Locate every Plasmodium falciparum-infected red blood cell.
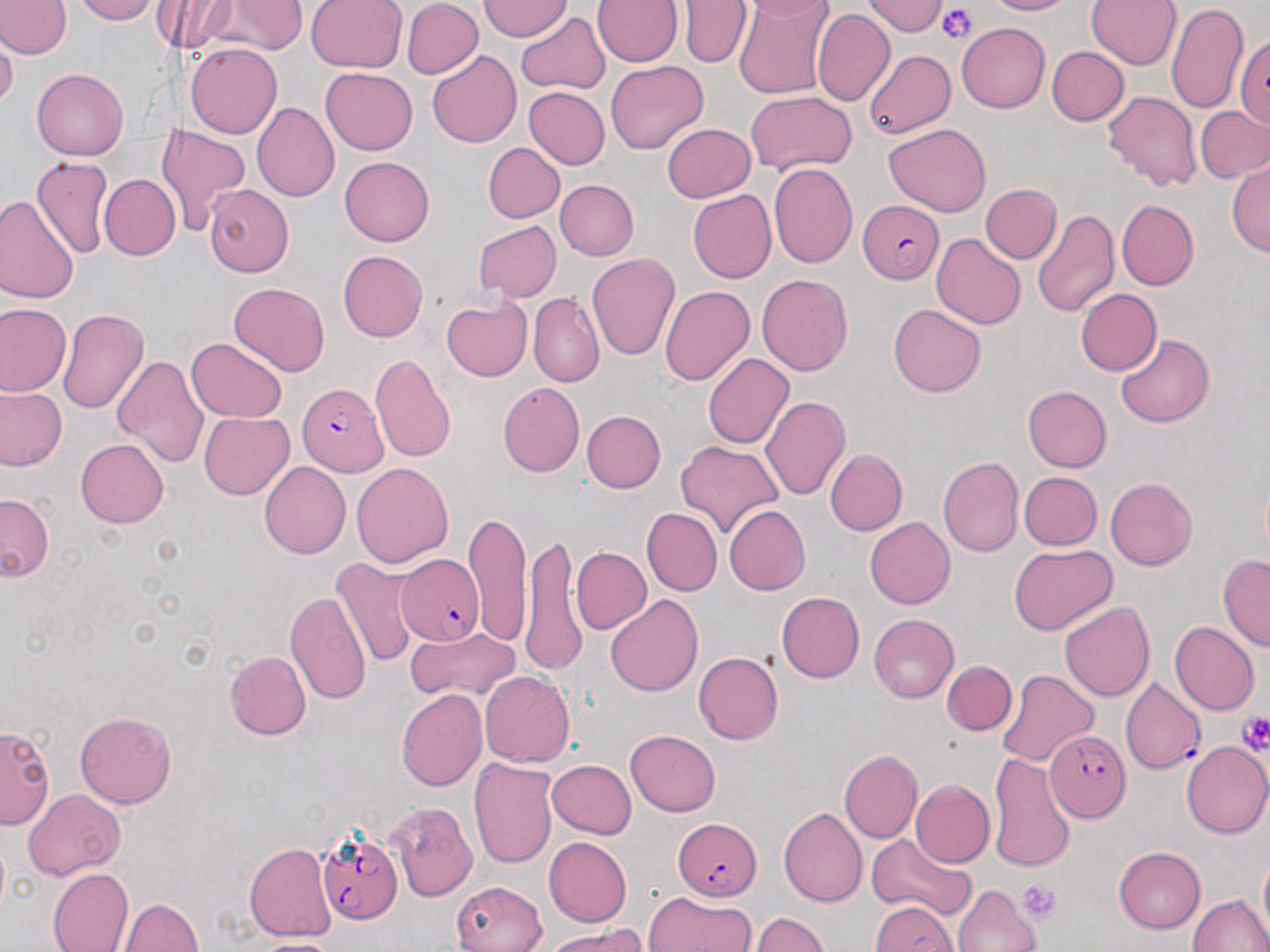
Approximate bounding boxes as named x1/y1/x2/y2 corners in pixels.
Plasmodium falciparum-infected red blood cells: (x1=855, y1=198, x2=942, y2=282), (x1=295, y1=382, x2=388, y2=473), (x1=394, y1=555, x2=484, y2=648), (x1=1122, y1=679, x2=1205, y2=776), (x1=1044, y1=731, x2=1130, y2=820), (x1=675, y1=817, x2=762, y2=900), (x1=314, y1=828, x2=401, y2=924).

Summary:
  - Platelet locations: (x1=936, y1=7, x2=979, y2=44), (x1=1236, y1=707, x2=1270, y2=760), (x1=1021, y1=880, x2=1060, y2=924)
  - Uninfected red blood cell locations: (x1=72, y1=0, x2=162, y2=24), (x1=154, y1=0, x2=250, y2=52), (x1=221, y1=0, x2=304, y2=53), (x1=306, y1=0, x2=406, y2=74), (x1=480, y1=0, x2=572, y2=41), (x1=593, y1=0, x2=683, y2=67), (x1=731, y1=0, x2=834, y2=100), (x1=868, y1=0, x2=945, y2=36), (x1=983, y1=0, x2=1075, y2=17), (x1=1087, y1=0, x2=1179, y2=71), (x1=401, y1=1, x2=481, y2=78), (x1=681, y1=1, x2=750, y2=67), (x1=0, y1=2, x2=68, y2=59), (x1=1167, y1=5, x2=1250, y2=116), (x1=517, y1=10, x2=610, y2=93), (x1=812, y1=10, x2=893, y2=108), (x1=957, y1=23, x2=1051, y2=112), (x1=1235, y1=31, x2=1270, y2=132), (x1=0, y1=41, x2=16, y2=110), (x1=185, y1=44, x2=280, y2=139), (x1=1046, y1=45, x2=1128, y2=125), (x1=864, y1=49, x2=955, y2=140), (x1=427, y1=50, x2=523, y2=145), (x1=605, y1=61, x2=708, y2=153), (x1=32, y1=68, x2=129, y2=160), (x1=321, y1=69, x2=417, y2=154), (x1=522, y1=86, x2=607, y2=171), (x1=1100, y1=88, x2=1202, y2=192), (x1=743, y1=93, x2=856, y2=176), (x1=251, y1=103, x2=337, y2=203), (x1=1195, y1=104, x2=1270, y2=184), (x1=154, y1=122, x2=250, y2=238), (x1=661, y1=123, x2=756, y2=203), (x1=883, y1=123, x2=992, y2=216), (x1=482, y1=142, x2=563, y2=223), (x1=339, y1=156, x2=435, y2=247), (x1=31, y1=157, x2=114, y2=258), (x1=1227, y1=157, x2=1269, y2=258), (x1=770, y1=162, x2=858, y2=271), (x1=97, y1=174, x2=179, y2=261), (x1=554, y1=177, x2=637, y2=259), (x1=980, y1=183, x2=1061, y2=264), (x1=202, y1=185, x2=295, y2=276), (x1=689, y1=189, x2=776, y2=282), (x1=0, y1=195, x2=80, y2=306), (x1=1115, y1=200, x2=1197, y2=292), (x1=1032, y1=207, x2=1120, y2=320), (x1=472, y1=220, x2=560, y2=300), (x1=932, y1=232, x2=1026, y2=330), (x1=340, y1=249, x2=430, y2=342), (x1=586, y1=253, x2=681, y2=360), (x1=755, y1=271, x2=853, y2=378), (x1=229, y1=284, x2=330, y2=377), (x1=659, y1=284, x2=753, y2=385), (x1=1074, y1=288, x2=1160, y2=374), (x1=527, y1=292, x2=604, y2=388), (x1=442, y1=296, x2=531, y2=381), (x1=1, y1=302, x2=71, y2=397), (x1=888, y1=304, x2=988, y2=398), (x1=58, y1=306, x2=149, y2=418), (x1=1116, y1=333, x2=1216, y2=428), (x1=186, y1=338, x2=289, y2=423), (x1=702, y1=352, x2=794, y2=450), (x1=111, y1=353, x2=209, y2=469), (x1=370, y1=354, x2=456, y2=462), (x1=499, y1=382, x2=584, y2=476), (x1=1023, y1=386, x2=1113, y2=472), (x1=0, y1=387, x2=67, y2=473), (x1=762, y1=395, x2=851, y2=501), (x1=582, y1=410, x2=666, y2=492), (x1=197, y1=411, x2=294, y2=499), (x1=76, y1=439, x2=168, y2=527), (x1=675, y1=439, x2=784, y2=538), (x1=825, y1=448, x2=906, y2=535), (x1=936, y1=457, x2=1022, y2=558), (x1=352, y1=461, x2=453, y2=568), (x1=260, y1=462, x2=351, y2=558), (x1=1020, y1=472, x2=1101, y2=550), (x1=1104, y1=477, x2=1197, y2=570), (x1=0, y1=494, x2=54, y2=585), (x1=723, y1=504, x2=812, y2=595), (x1=642, y1=508, x2=722, y2=595), (x1=466, y1=513, x2=533, y2=643), (x1=866, y1=516, x2=955, y2=609), (x1=524, y1=535, x2=587, y2=677), (x1=1008, y1=543, x2=1117, y2=635), (x1=570, y1=545, x2=651, y2=635), (x1=1218, y1=554, x2=1269, y2=650), (x1=332, y1=556, x2=419, y2=673), (x1=284, y1=588, x2=373, y2=708), (x1=777, y1=591, x2=865, y2=682), (x1=606, y1=593, x2=702, y2=696), (x1=1058, y1=600, x2=1156, y2=703), (x1=866, y1=614, x2=958, y2=703), (x1=1170, y1=621, x2=1259, y2=713), (x1=403, y1=623, x2=523, y2=705), (x1=224, y1=651, x2=311, y2=740), (x1=694, y1=651, x2=784, y2=745), (x1=942, y1=661, x2=1016, y2=736), (x1=995, y1=669, x2=1099, y2=771), (x1=479, y1=671, x2=573, y2=769), (x1=395, y1=688, x2=488, y2=794), (x1=74, y1=710, x2=178, y2=808), (x1=2, y1=720, x2=54, y2=832), (x1=625, y1=729, x2=721, y2=817), (x1=1182, y1=741, x2=1270, y2=840), (x1=839, y1=748, x2=922, y2=843), (x1=987, y1=752, x2=1077, y2=870), (x1=470, y1=758, x2=559, y2=871), (x1=548, y1=759, x2=637, y2=838), (x1=910, y1=779, x2=994, y2=866), (x1=24, y1=790, x2=124, y2=882), (x1=385, y1=801, x2=480, y2=902), (x1=778, y1=808, x2=867, y2=906), (x1=865, y1=832, x2=975, y2=918), (x1=545, y1=836, x2=633, y2=926), (x1=242, y1=840, x2=338, y2=940), (x1=1113, y1=846, x2=1207, y2=933), (x1=1255, y1=855, x2=1269, y2=929), (x1=48, y1=867, x2=132, y2=952), (x1=451, y1=878, x2=546, y2=952), (x1=952, y1=884, x2=1040, y2=952), (x1=1184, y1=889, x2=1270, y2=952), (x1=646, y1=892, x2=759, y2=952), (x1=121, y1=897, x2=205, y2=952), (x1=868, y1=900, x2=957, y2=952), (x1=752, y1=910, x2=831, y2=952), (x1=542, y1=927, x2=650, y2=950), (x1=246, y1=936, x2=349, y2=952)
  - Slide-level diagnosis: Plasmodium falciparum
  - Image size: 1270×952 pixels
  - Magnification: 1000x
  - Preparation: thin blood smear
  - Field of view: single
  - Modality: optical microscopy
  - Stain: May-Grünwald-Giemsa